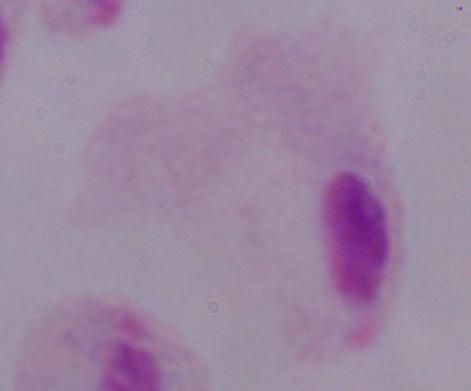

Photomicrograph. Captured at 1000x magnification. A trichomonad is seen.